State which parasite is depicted.
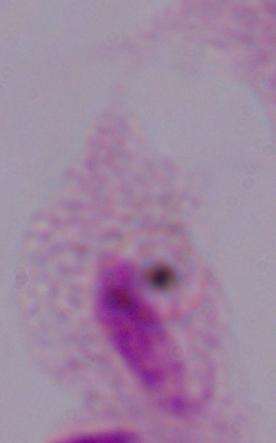
A trichomonad.

modality = micrograph
magnification = 1000x